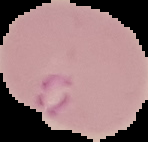

Summary:
  - Preparation: thin blood film
  - Result: malaria parasites identified
  - Image size: 148×142 pixels
  - Image type: cell region segmented out of the field of view; surrounding area masked to black